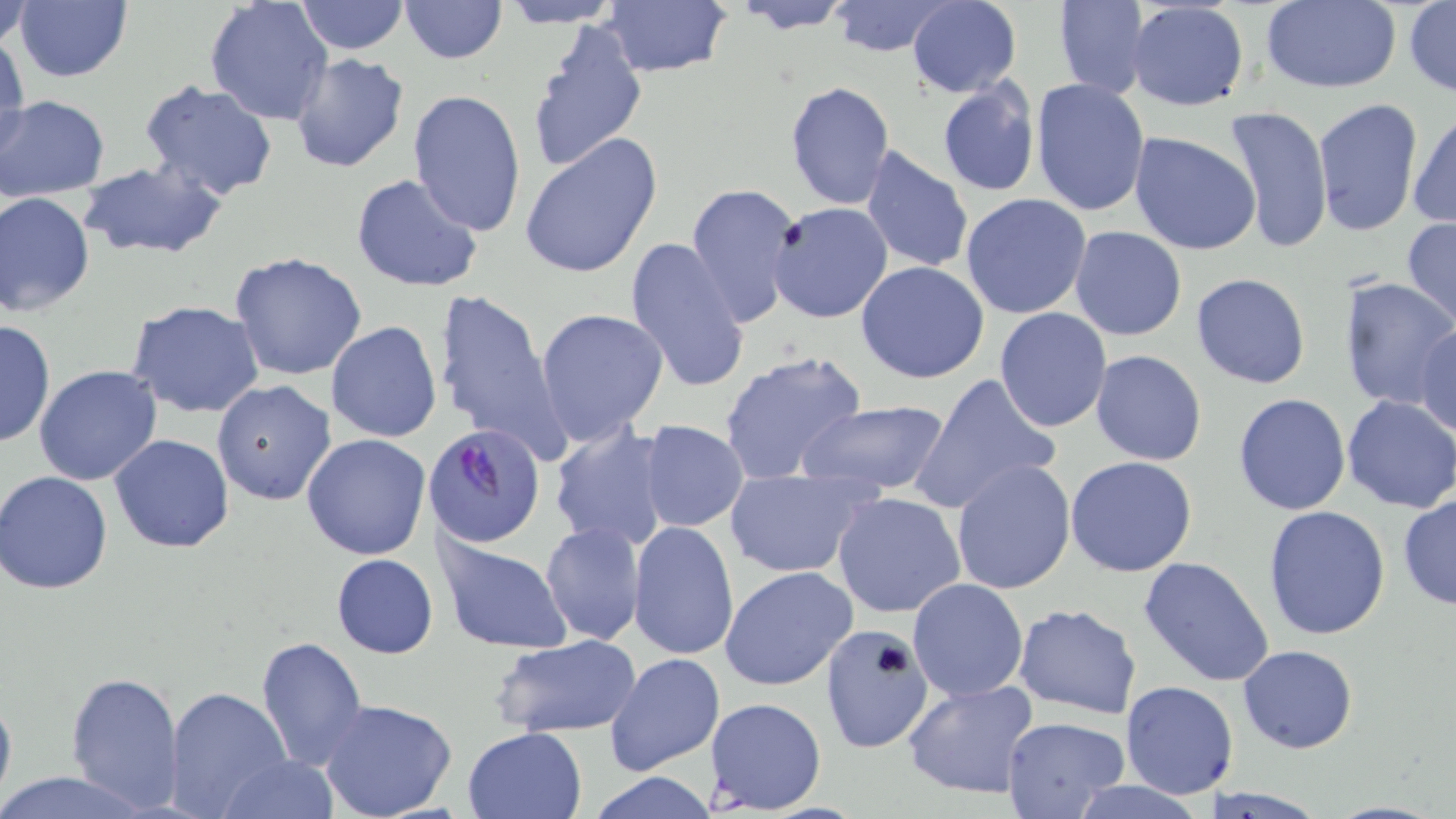
Summary:
  - Coordinate format: approximate bounding boxes as (x1,y1)-(x2,y2) corner pairs in pixels
  - Uninfected red blood cell locations: (1,0)-(31,49), (13,0)-(133,84), (295,0)-(407,54), (399,0)-(506,64), (728,0)-(858,33), (1053,0)-(1150,100), (1259,0)-(1401,92), (205,1)-(332,124), (498,1)-(622,27), (826,1)-(959,59), (907,1)-(1021,97), (601,2)-(731,79), (1125,2)-(1250,113), (1404,2)-(1455,98), (526,16)-(648,177), (1,32)-(28,158), (288,53)-(410,175), (937,78)-(1040,197), (1030,78)-(1149,218), (136,80)-(281,203), (786,80)-(896,213), (406,89)-(527,236), (1,96)-(109,200), (1313,98)-(1422,236), (1224,105)-(1334,259), (1407,111)-(1455,229), (1129,132)-(1261,256), (519,133)-(664,279), (860,146)-(974,271), (79,159)-(228,258), (350,173)-(483,292), (686,182)-(801,330), (0,191)-(96,317), (960,193)-(1093,320), (766,202)-(893,323), (1401,218)-(1456,328), (1069,225)-(1187,343), (624,237)-(751,395), (229,251)-(368,380), (856,261)-(991,384), (1191,273)-(1310,388), (1338,276)-(1455,411), (432,287)-(568,467), (126,302)-(264,418), (536,307)-(669,445), (994,307)-(1112,433), (0,318)-(55,451), (326,321)-(443,442), (1413,323)-(1456,439), (717,349)-(870,487), (1088,350)-(1207,465), (33,365)-(162,485), (909,373)-(1060,511), (211,379)-(336,505), (1232,393)-(1352,515), (1340,396)-(1456,512), (797,399)-(953,498), (640,420)-(750,533), (550,424)-(671,554), (302,433)-(432,561), (110,434)-(236,554), (1065,455)-(1198,577), (950,458)-(1077,596), (724,466)-(877,578), (2,471)-(116,594), (831,491)-(966,619), (1397,494)-(1456,611), (1263,505)-(1391,641), (628,521)-(739,662), (540,523)-(644,646), (438,537)-(573,653), (331,553)-(438,659), (1138,556)-(1276,688), (720,565)-(858,691), (907,577)-(1030,702), (1013,603)-(1141,717), (820,626)-(935,756), (491,635)-(641,738), (256,636)-(368,769), (1238,645)-(1356,753), (604,652)-(725,776), (66,670)-(183,810), (901,679)-(1039,800), (1121,681)-(1239,799), (164,685)-(292,817), (0,688)-(16,809), (705,697)-(827,815), (318,698)-(459,819), (1000,716)-(1130,819), (463,728)-(586,818), (219,754)-(338,819), (588,770)-(717,818), (0,771)-(159,818), (1065,780)-(1212,819), (1199,787)-(1331,819)
  - Plasmodium falciparum-infected red blood cell locations: (424,424)-(546,547)
  - Slide-level diagnosis: Plasmodium falciparum
  - Magnification: 1000x
  - Stain: May-Grünwald-Giemsa
  - Field of view: single
  - Modality: optical microscopy
  - Image size: 1456×819 pixels
  - Preparation: thin blood film